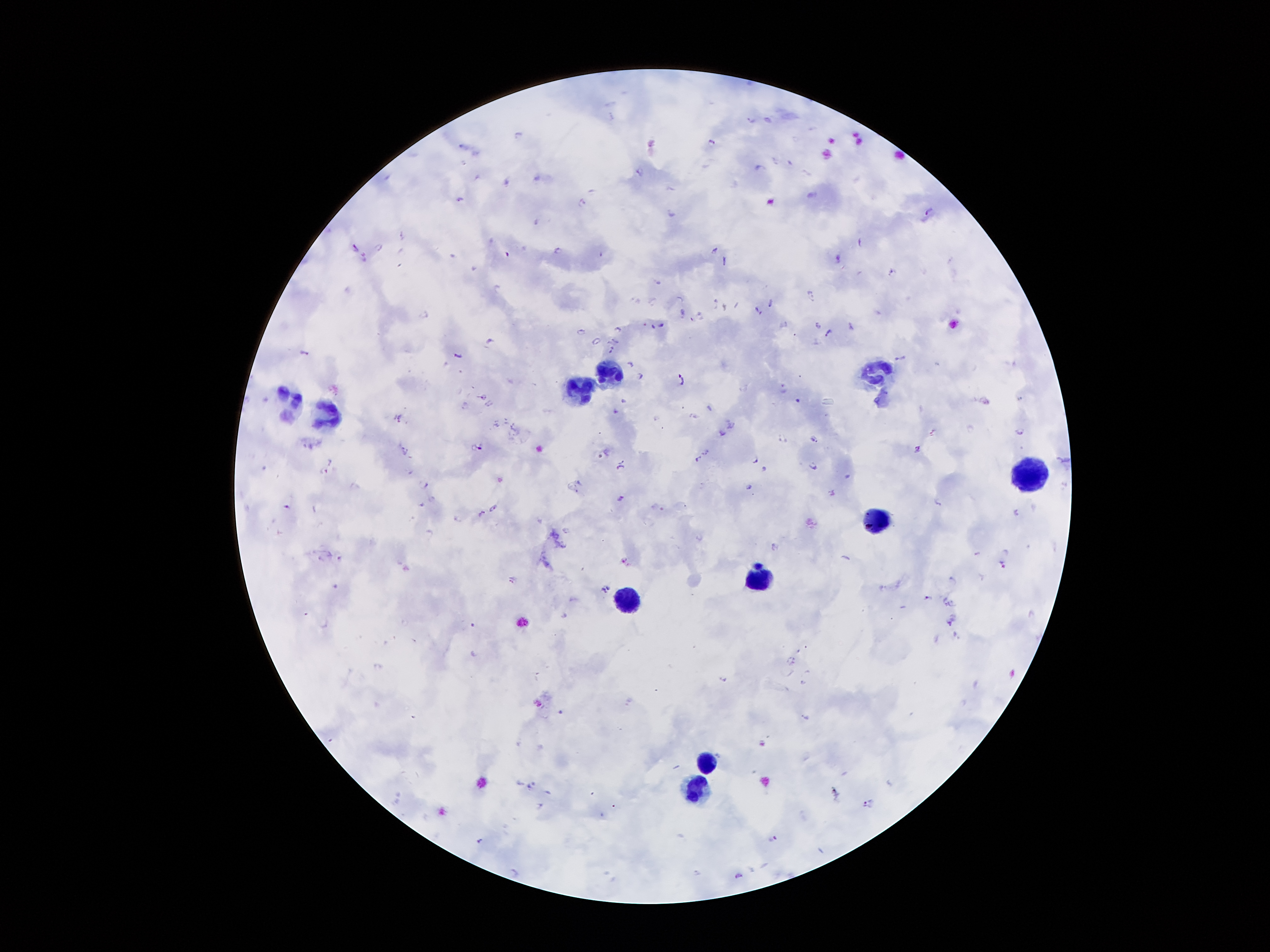

Approximate centers as {x, y} in pixels. Plasmodium parasite locations: {750, 119}, {520, 134}, {711, 140}, {463, 145}, {789, 161}, {758, 165}, {640, 168}, {506, 180}, {672, 188}, {458, 199}, {584, 199}, {928, 212}, {670, 214}, {535, 221}, {861, 241}, {380, 246}, {356, 248}, {557, 250}, {716, 250}, {724, 260}, {890, 271}, {659, 283}, {810, 293}, {715, 301}, {770, 304}, {725, 306}, {756, 310}, {682, 312}, {422, 313}, {700, 315}, {817, 324}, {663, 325}, {849, 326}, {617, 327}, {653, 327}, {581, 331}, {828, 333}, {595, 339}, {491, 342}, {613, 342}, {612, 350}, {302, 352}, {457, 354}, {899, 358}, {630, 363}, {639, 376}, {682, 381}, {783, 389}, {1020, 399}, {625, 401}, {796, 401}, {709, 407}, {615, 411}, {399, 415}, {694, 417}, {730, 424}, {932, 431}, {721, 432}, {1019, 432}, {815, 438}, {781, 439}, {311, 440}, {478, 443}, {914, 447}, {405, 449}, {605, 450}, {707, 451}, {700, 459}, {756, 460}, {324, 465}, {619, 465}, {811, 466}, {767, 469}, {849, 477}, {427, 484}, {750, 489}, {834, 493}, {620, 498}, {431, 500}, {936, 500}, {283, 502}, {492, 507}, {481, 511}, {1017, 511}, {457, 516}, {566, 528}, {430, 530}, {698, 537}, {774, 546}, {339, 554}, {975, 554}, {624, 561}, {1001, 565}, {512, 578}, {952, 578}, {605, 587}, {926, 597}, {948, 601}, {950, 622}, {794, 659}, {723, 678}, {803, 682}, {536, 702}, {560, 711}, {804, 716}, {762, 743}, {531, 784}, {832, 791}, {538, 803}, {868, 803}, {773, 837}, {480, 841}, {514, 871}, {738, 874}. Leukocyte locations: {878, 367}, {610, 371}, {580, 390}, {291, 403}, {330, 414}, {1030, 472}, {872, 520}, {762, 578}, {623, 600}, {707, 761}, {698, 788}. Patient malaria status: positive for Plasmodium falciparum. Image is 1270×952 pixels. 100x magnification. Photographed through the microscope eyepiece with a smartphone camera. One field from this slide. Thick blood film. Giemsa-stained preparation.